Name the parasite shown.
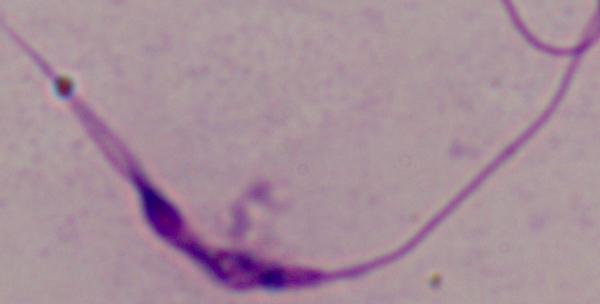

This is Leishmania.

Summary:
  - Modality: photomicrograph
  - Magnification: 1000x